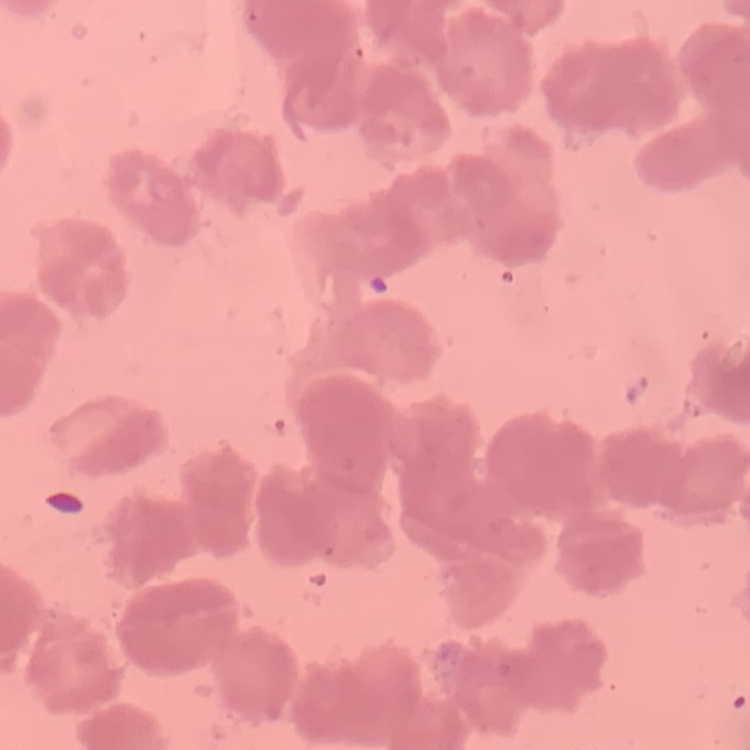

erythrocyte morphology = rouleaux formation
image type = square crop of a larger photomicrograph
preparation = thin blood smear
stain = Field's or Giemsa